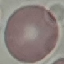

Summary:
  - Result: negative for malaria parasites
  - Image type: automatically extracted cell patch, resized to 64 × 64 pixels
  - Preparation: thin blood film
  - Capture: smartphone camera at the microscope eyepiece
  - Stain: Giemsa